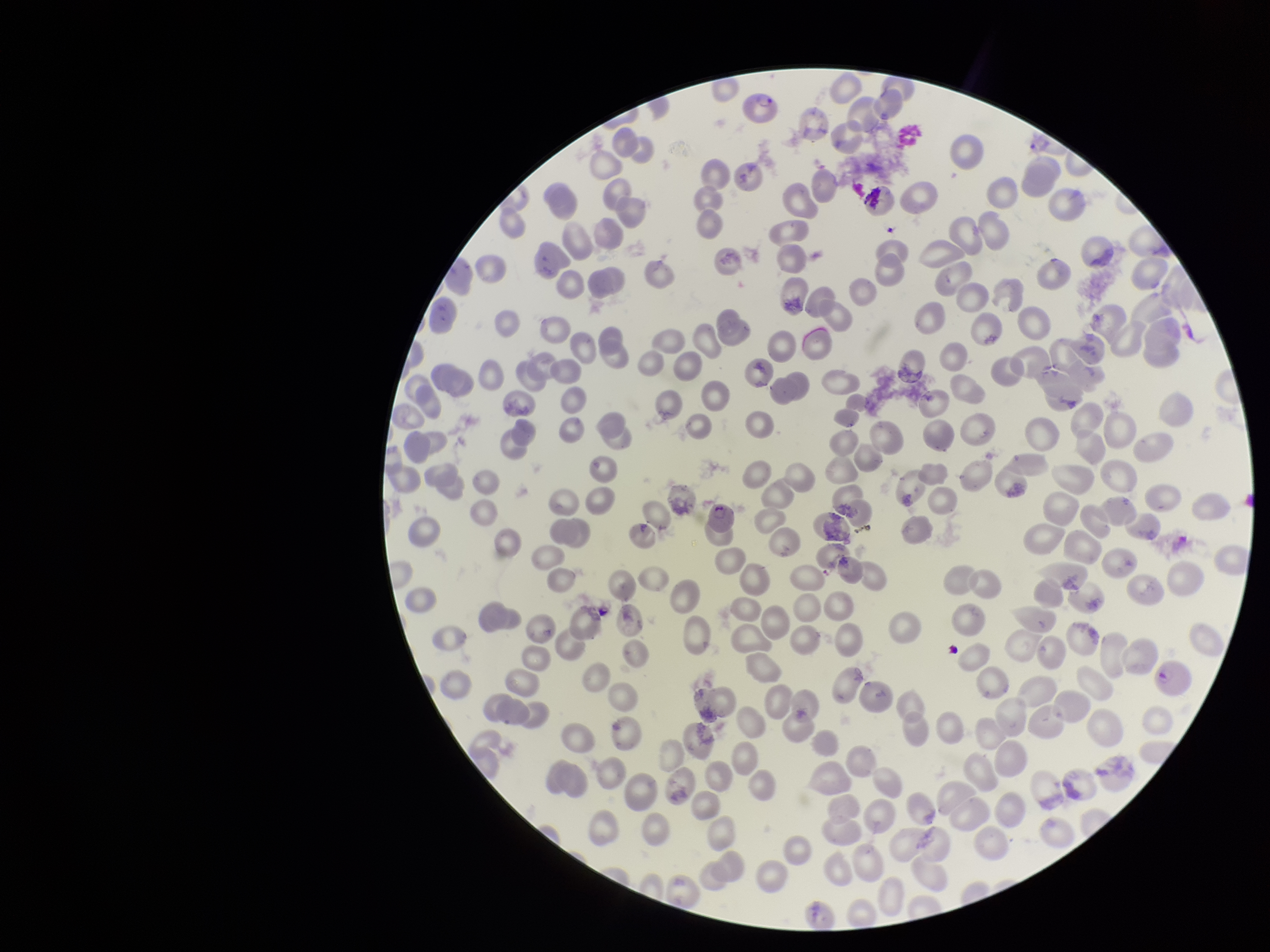 Preparation: thin blood smear. Stained with Giemsa. Single field of view. Patient malaria status: positive. Photographed through the microscope eyepiece with a smartphone camera. Image is 1270×952 pixels. Parasitized red blood cells: identified. Species reported for this patient: Plasmodium falciparum. Parasitized red blood cell count: 3. Red blood cell count: 222.